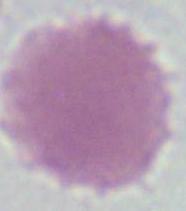 An erythrocyte is seen. Micrograph. Captured at 1000x magnification.